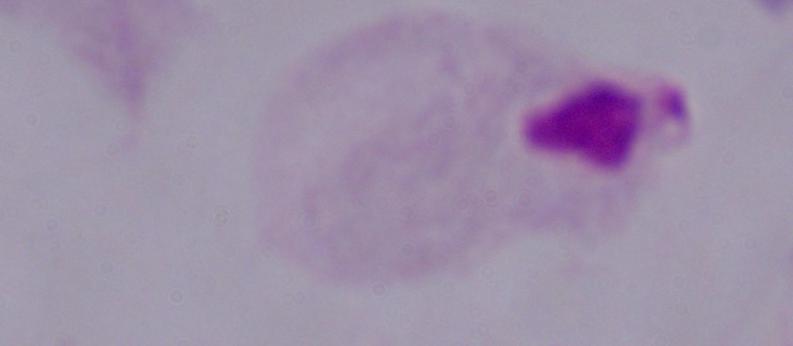

magnification = 1000x
identification = trichomonad
modality = micrograph